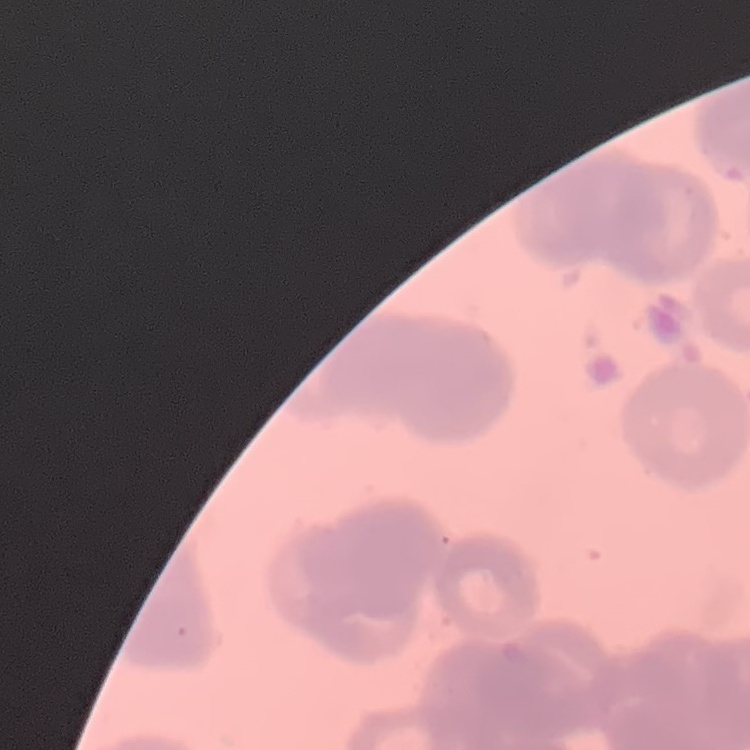
The red blood cells show rouleaux formation. Thin blood smear. Square crop of a larger photomicrograph. Field's or Giemsa stain.